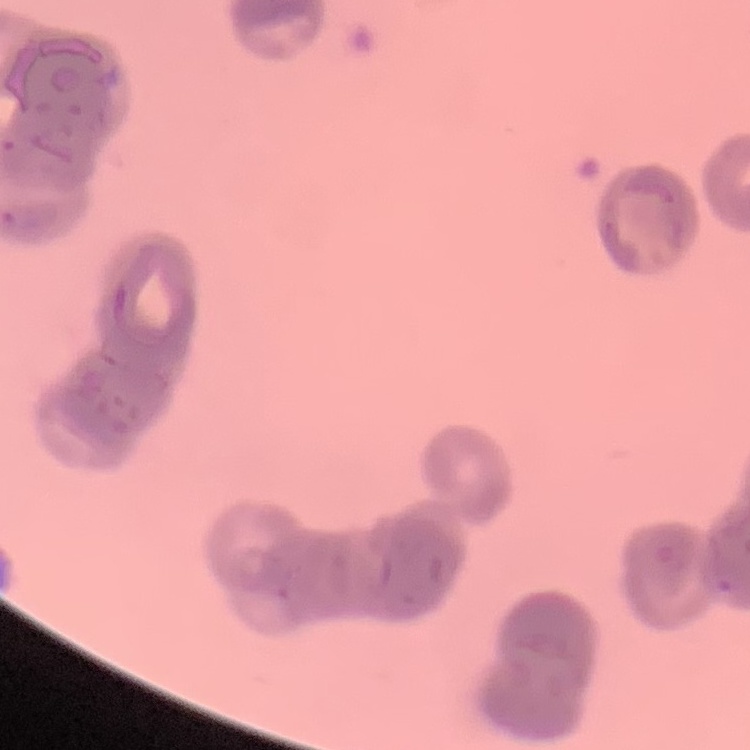
erythrocyte morphology = rouleaux formation
preparation = thin peripheral smear
image type = one tile cut from a larger photomicrograph
stain = Field's or Giemsa